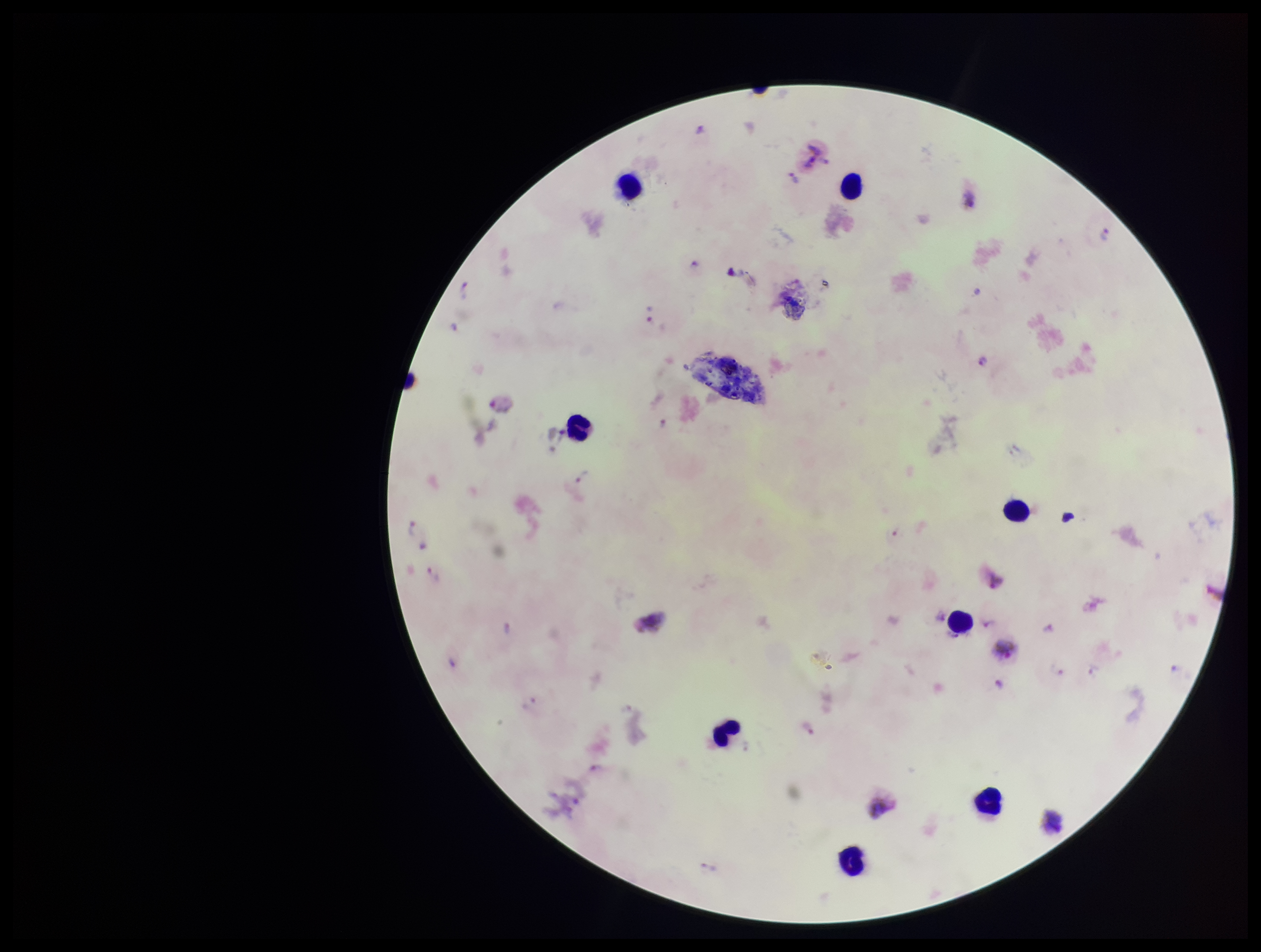
stain: Giemsa
patient_malaria_status: infected
plasmodium_parasites: detected
preparation: thick
species_reported_for_this_patient: Plasmodium vivax
image_size: 1261×952 pixels
capture: smartphone photograph through the microscope eyepiece
field_of_view: one from this slide
parasite_count: 11
leukocyte_count: 8